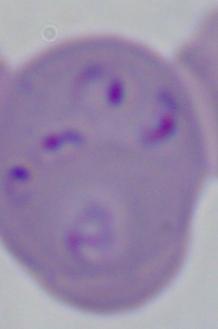

modality = photomicrograph
magnification = 1000x
identification = Babesia